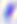

Summary:
  - Identification: Toxoplasma gondii
  - Modality: photomicrograph
  - Magnification: 400x